Give the extent of all uninfected red blood cells.
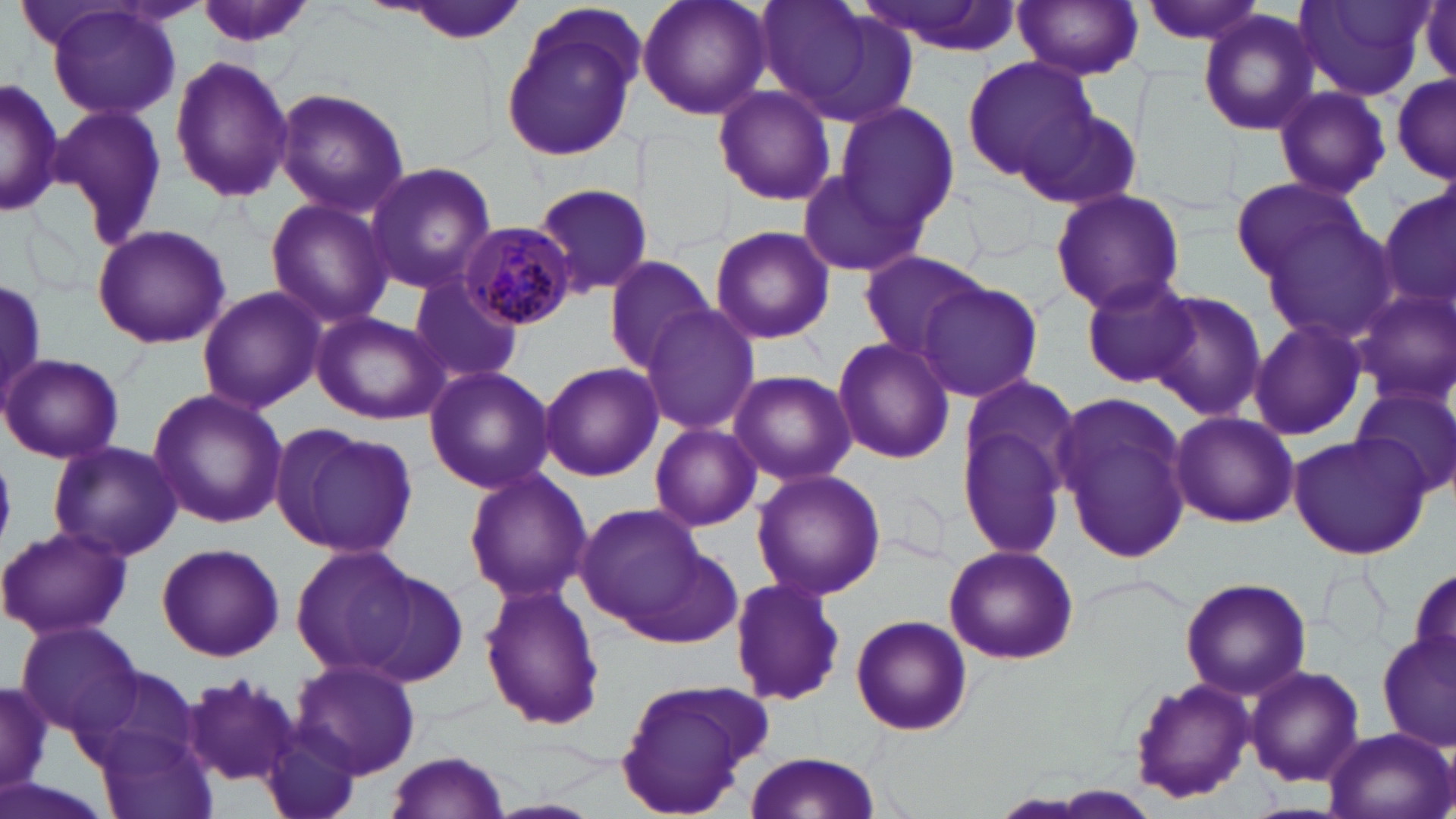

Approximate bounding boxes as [x1, y1, x2, y2] in pixels.
Uninfected red blood cells: [192, 0, 318, 53], [636, 0, 773, 122], [753, 0, 912, 124], [858, 0, 1024, 56], [1014, 0, 1143, 81], [1134, 0, 1270, 48], [1418, 0, 1455, 91], [392, 1, 527, 45], [1296, 1, 1429, 100], [44, 4, 185, 122], [499, 6, 647, 159], [1197, 8, 1320, 138], [168, 55, 295, 202], [960, 56, 1096, 184], [1390, 72, 1454, 186], [0, 76, 64, 218], [711, 85, 837, 206], [1273, 86, 1391, 201], [274, 88, 409, 215], [831, 101, 959, 233], [47, 102, 169, 249], [1022, 107, 1142, 210], [364, 161, 496, 294], [796, 170, 927, 278], [1230, 179, 1372, 284], [535, 183, 656, 299], [1379, 185, 1456, 319], [1048, 187, 1186, 315], [263, 197, 394, 332], [1257, 213, 1400, 345], [90, 223, 232, 351], [708, 224, 836, 346], [858, 252, 995, 357], [603, 255, 718, 374], [408, 272, 525, 388], [1078, 274, 1202, 388], [916, 279, 1044, 404], [0, 282, 47, 410], [195, 285, 328, 415], [1352, 288, 1456, 410], [1150, 290, 1267, 423], [639, 305, 761, 434], [312, 311, 450, 425], [1246, 316, 1369, 444], [830, 336, 956, 465], [2, 353, 123, 463], [538, 361, 663, 482], [423, 366, 556, 494], [727, 369, 855, 485], [953, 376, 1083, 563], [1347, 384, 1456, 499], [146, 387, 289, 530], [1053, 389, 1195, 565], [1170, 412, 1301, 528], [648, 421, 762, 531], [271, 423, 417, 560], [1287, 432, 1431, 560], [47, 440, 185, 561], [751, 468, 885, 602], [462, 469, 591, 606], [572, 504, 710, 632], [0, 525, 133, 641], [617, 541, 746, 652], [156, 543, 286, 662], [290, 544, 416, 676], [943, 544, 1078, 664], [1409, 566, 1456, 680], [357, 569, 470, 690], [727, 576, 847, 707], [1179, 576, 1313, 700], [477, 585, 606, 731], [850, 613, 973, 735], [17, 621, 144, 736], [1378, 630, 1456, 753], [290, 658, 420, 778], [71, 665, 201, 773], [1245, 665, 1363, 785], [182, 673, 301, 786], [0, 674, 56, 793], [613, 674, 775, 815], [1130, 680, 1254, 802], [258, 723, 367, 819], [93, 725, 217, 819], [1322, 726, 1455, 819], [742, 748, 883, 816], [383, 750, 511, 818], [0, 777, 114, 819].

Summary:
  - Plasmodium malariae-infected red blood cell locations: [464, 222, 576, 329]
  - Slide-level diagnosis: Plasmodium malariae
  - Field of view: one of a larger specimen
  - Preparation: thin blood film
  - Image size: 1456×819 pixels
  - Stain: May-Grünwald-Giemsa
  - Magnification: 1000x
  - Modality: light microscopy